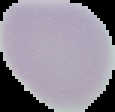
Malaria status: uninfected. Image is 115×112 pixels. From a thin blood film. The area outside the segmented cell region is set to black.